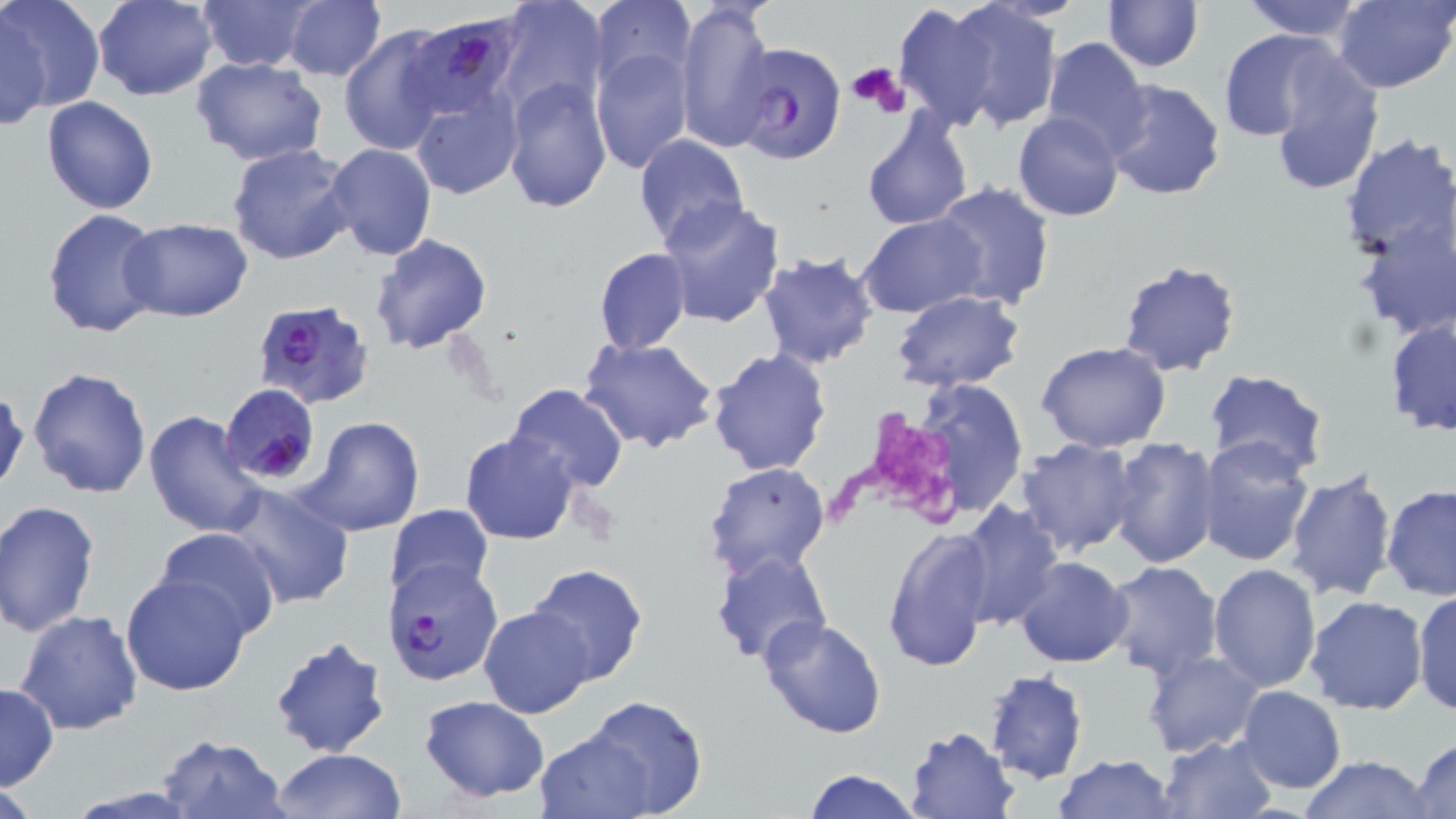

slide-level diagnosis = Plasmodium falciparum
preparation = thin blood smear
Plasmodium falciparum-infected red blood cell locations = approximate bounding boxes as (x1,y1)-(x2,y2) corner pairs in pixels: (401,10)-(528,119), (732,42)-(848,164), (252,300)-(375,410), (219,382)-(319,485), (383,558)-(503,685)
platelet locations = approximate bounding boxes as (x1,y1)-(x2,y2) corner pairs in pixels: (848,63)-(908,114), (865,413)-(956,512)
image size = 1456×819 pixels
stain = May-Grünwald-Giemsa
modality = optical microscopy
field of view = one of a larger specimen
uninfected red blood cell locations = approximate bounding boxes as (x1,y1)-(x2,y2) corner pairs in pixels: (0,0)-(104,113), (94,0)-(217,100), (195,0)-(321,71), (587,0)-(695,94), (674,0)-(774,150), (1102,0)-(1202,71), (1239,0)-(1368,40), (1332,0)-(1456,93), (892,1)-(1001,131), (282,2)-(383,80), (493,2)-(610,114), (947,2)-(1061,131), (0,8)-(47,131), (581,25)-(769,163), (339,26)-(449,153), (1217,30)-(1343,142), (1041,37)-(1151,156), (591,47)-(694,174), (1269,54)-(1387,195), (191,57)-(329,166), (502,75)-(612,212), (1100,77)-(1227,201), (407,89)-(522,201), (42,96)-(159,216), (1014,111)-(1124,221), (861,113)-(973,230), (630,136)-(747,247), (1341,137)-(1454,261), (226,142)-(356,266), (323,144)-(436,261), (930,182)-(1057,312), (656,196)-(785,328), (42,208)-(164,339), (858,214)-(989,318), (120,216)-(254,321), (1353,220)-(1455,339), (369,234)-(491,354), (594,247)-(690,353), (756,249)-(882,371), (1116,259)-(1243,378), (889,291)-(1025,392), (1384,317)-(1455,436), (577,337)-(720,456), (1037,341)-(1172,454), (706,348)-(833,477), (27,366)-(153,501), (1202,368)-(1329,483), (911,378)-(1030,517), (505,384)-(628,493), (0,388)-(28,496), (142,411)-(266,538), (299,417)-(424,537), (460,430)-(582,546), (1107,437)-(1221,569), (1014,438)-(1141,557), (1196,439)-(1316,567), (703,461)-(831,581), (1284,469)-(1398,605), (220,481)-(357,608), (1381,485)-(1456,601), (0,501)-(100,635), (953,502)-(1062,628), (386,504)-(492,601), (153,527)-(281,640), (883,531)-(993,671), (711,547)-(833,670), (1015,556)-(1135,669), (1097,561)-(1223,681), (525,563)-(648,685), (1208,563)-(1321,693), (121,572)-(252,695), (1413,588)-(1455,718), (1304,595)-(1430,714), (480,603)-(595,718), (14,609)-(146,736), (759,615)-(888,739), (267,635)-(391,759), (1140,648)-(1265,758), (983,671)-(1089,785), (0,680)-(59,791), (1236,685)-(1346,793), (419,695)-(550,804), (569,695)-(708,818), (533,726)-(662,819), (905,727)-(1020,818), (155,732)-(290,819), (1157,735)-(1277,817), (1408,735)-(1456,819), (273,748)-(405,819), (1297,754)-(1436,819), (1052,755)-(1180,818), (800,767)-(924,819)
magnification = 1000x